Give the extent of all uninfected red blood cells.
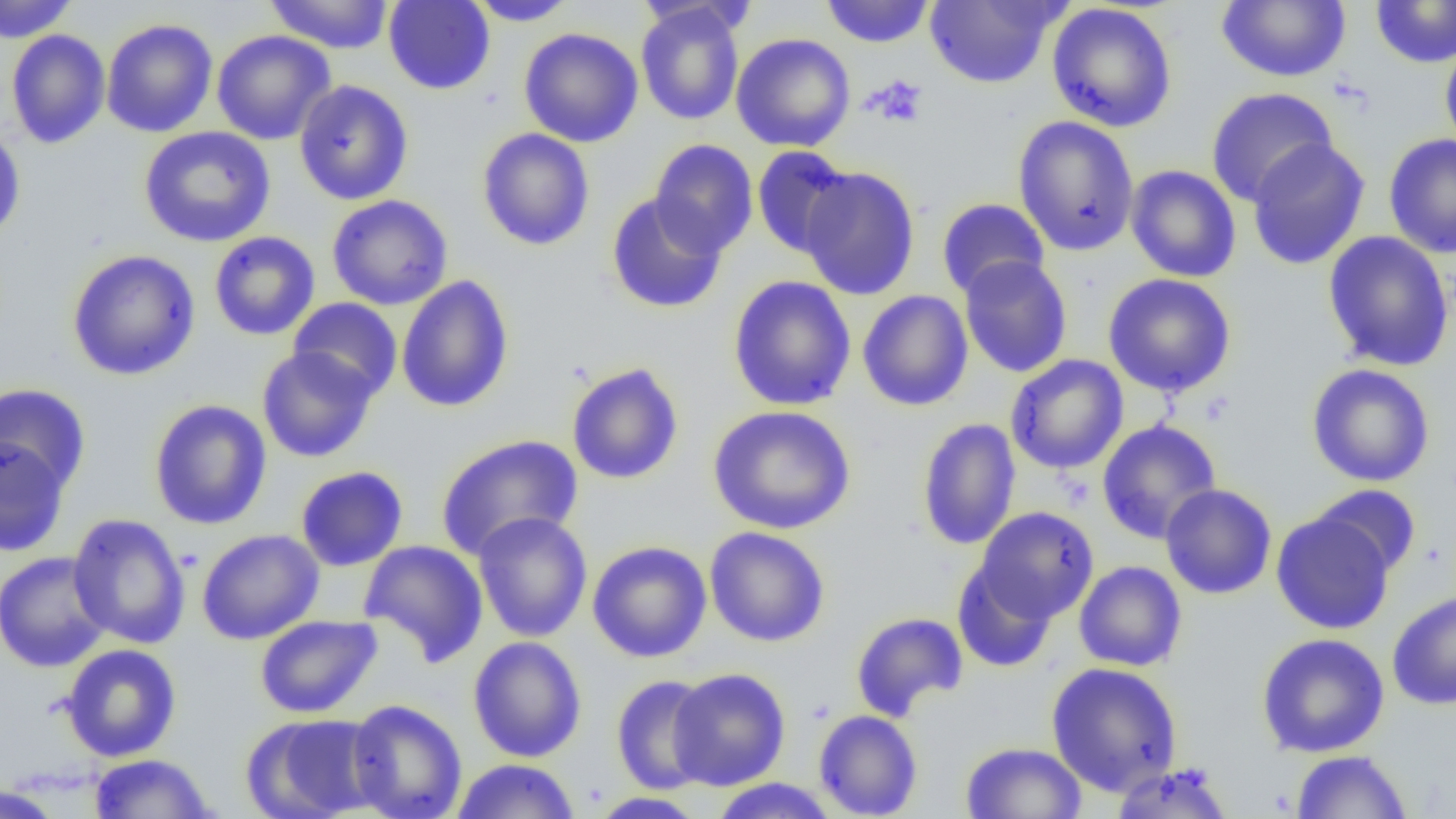

Approximate bounding boxes as [x1, y1, x2, y2] in pixels.
Uninfected red blood cells: [0, 0, 79, 43], [264, 0, 394, 54], [383, 0, 495, 95], [469, 0, 579, 26], [820, 0, 935, 48], [925, 0, 1063, 89], [1215, 0, 1351, 83], [1370, 1, 1456, 68], [1046, 2, 1178, 133], [636, 3, 745, 125], [102, 18, 218, 138], [519, 27, 644, 147], [6, 29, 110, 149], [212, 30, 336, 145], [731, 33, 856, 152], [1440, 39, 1456, 159], [294, 80, 413, 205], [1205, 87, 1339, 207], [1012, 115, 1140, 257], [0, 122, 26, 242], [139, 126, 275, 248], [477, 128, 595, 251], [1384, 133, 1456, 259], [1246, 138, 1370, 270], [649, 139, 758, 257], [751, 146, 855, 258], [1125, 164, 1241, 283], [798, 166, 920, 300], [605, 193, 727, 314], [326, 194, 453, 311], [936, 197, 1050, 299], [1322, 231, 1455, 372], [208, 232, 321, 341], [66, 249, 201, 381], [958, 255, 1073, 378], [1102, 273, 1236, 398], [395, 275, 514, 413], [727, 275, 857, 411], [857, 290, 973, 412], [288, 297, 402, 401], [256, 346, 379, 463], [1006, 354, 1129, 474], [566, 362, 684, 485], [1306, 364, 1436, 487], [0, 383, 91, 495], [148, 399, 272, 530], [707, 404, 856, 534], [916, 417, 1021, 551], [1096, 420, 1222, 544], [434, 433, 584, 561], [0, 436, 71, 557], [295, 465, 408, 571], [1159, 483, 1277, 599], [1310, 485, 1422, 580], [975, 507, 1099, 622], [1271, 509, 1395, 635], [472, 512, 592, 643], [67, 513, 191, 649], [704, 526, 831, 647], [197, 529, 324, 645], [358, 539, 488, 667], [587, 541, 712, 663], [0, 551, 112, 673], [952, 559, 1059, 672], [1073, 561, 1187, 671], [1387, 590, 1456, 710], [850, 611, 968, 722], [254, 615, 383, 719], [1256, 632, 1390, 758], [467, 636, 587, 762], [59, 643, 182, 762], [1045, 661, 1183, 796], [667, 668, 791, 791], [610, 674, 717, 794], [346, 699, 467, 819], [813, 709, 923, 818], [241, 713, 383, 819], [959, 741, 1087, 819], [1290, 750, 1413, 818], [88, 753, 216, 818], [451, 759, 581, 818], [1109, 762, 1235, 818], [709, 778, 840, 818], [1, 783, 66, 818], [587, 792, 708, 818].

Platelet locations: [867, 74, 929, 128]. Slide-level diagnosis: negative for blood parasites. Optical microscopy. Thin blood film. 1000x magnification. Image is 1456×819 pixels. Single field of view.